Report the malaria status.
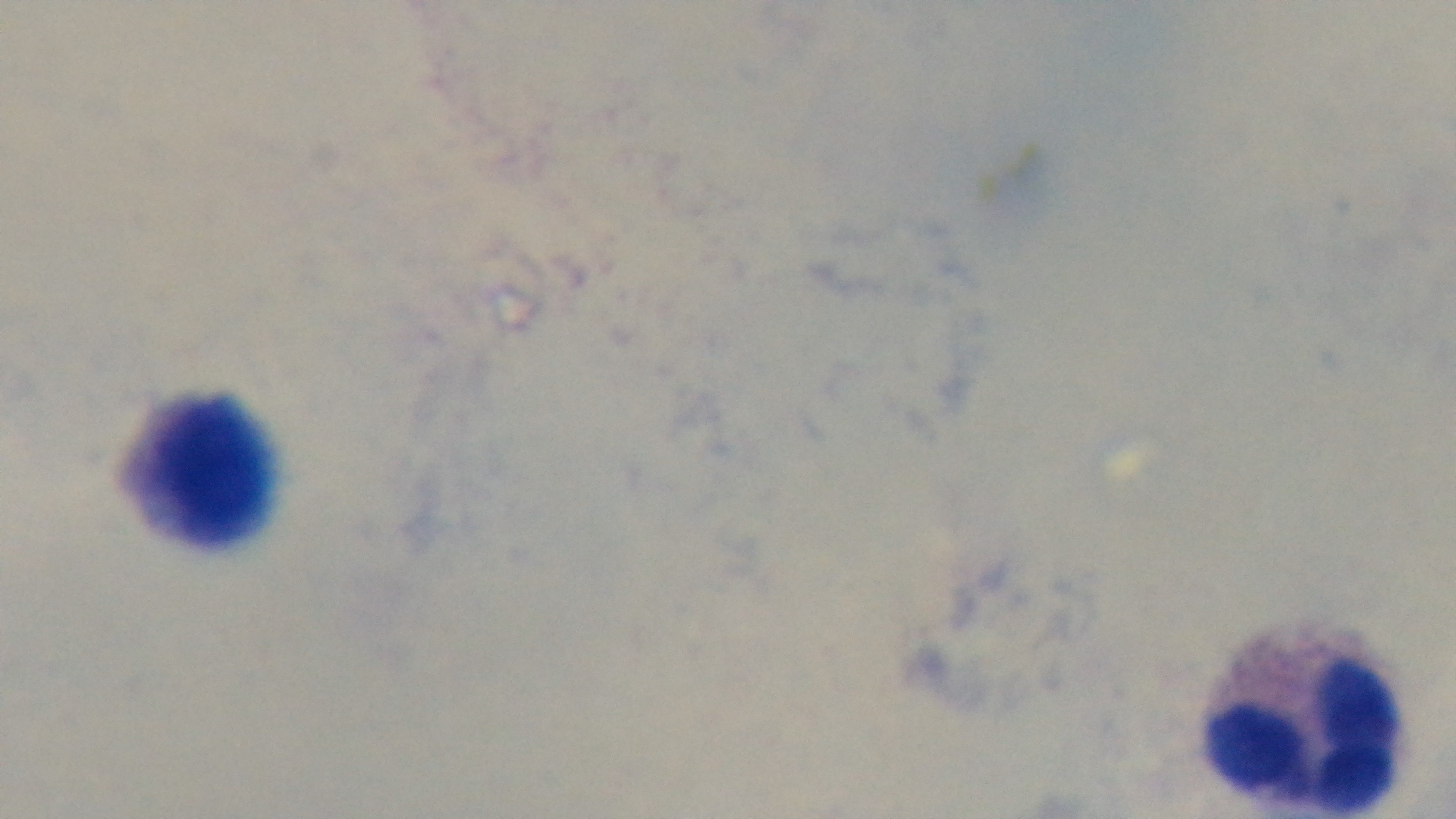

Uninfected.

Oil-immersion objective, 100x. Light microscopy. Giemsa stain. Mounted 4K digital camera. Preparation: thick smear. Single field of view.